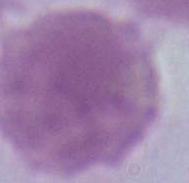

Summary:
  - Identification: red blood cell
  - Modality: photomicrograph
  - Magnification: 1000x